Report the malaria status of this cell.
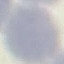

It is uninfected.

Giemsa-stained preparation. Thin blood film. Cell patch, automatically extracted from a larger field of view and resized to 64 × 64 pixels. Acquired by smartphone through the microscope eyepiece.